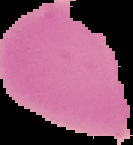

Summary:
  - Result: negative for Plasmodium parasites
  - Image type: cell region segmented out of the field of view; surrounding area masked to black
  - Preparation: thin blood smear
  - Image size: 133×145 pixels